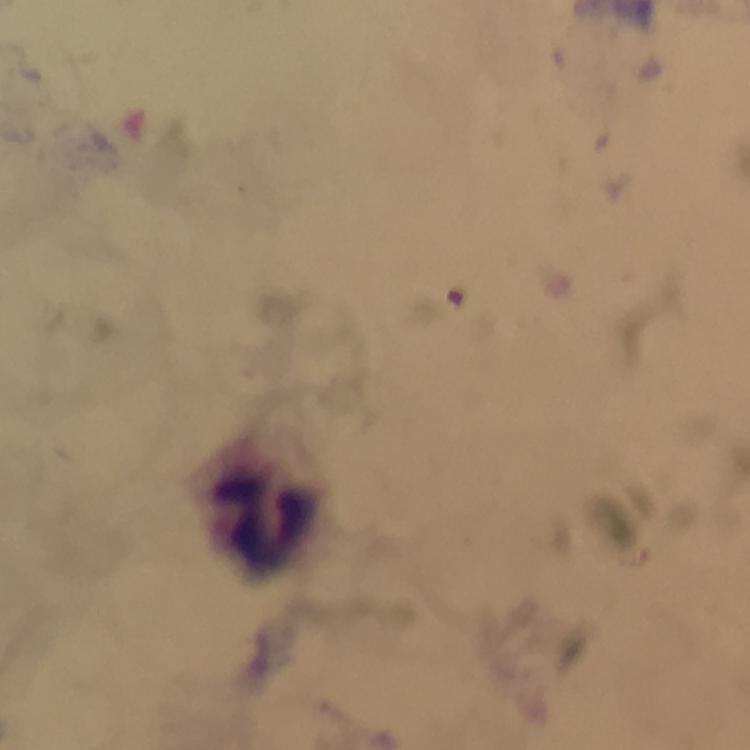
Approximate centers as (x, y) in pixels.
Summary:
  - Leukocyte locations: (265, 519)
  - Context: from a malaria diagnostic workup
  - Cropped from: one field of view
  - Immersion oil: applied
  - Magnification: 100x
  - Capture: smartphone mounted on the microscope
  - Stain: Giemsa
  - Malaria parasites: none detected
  - Preparation: thick blood film
  - Image size: 750×750 pixels